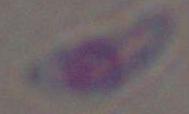

modality = micrograph
identification = Toxoplasma gondii
magnification = 1000x